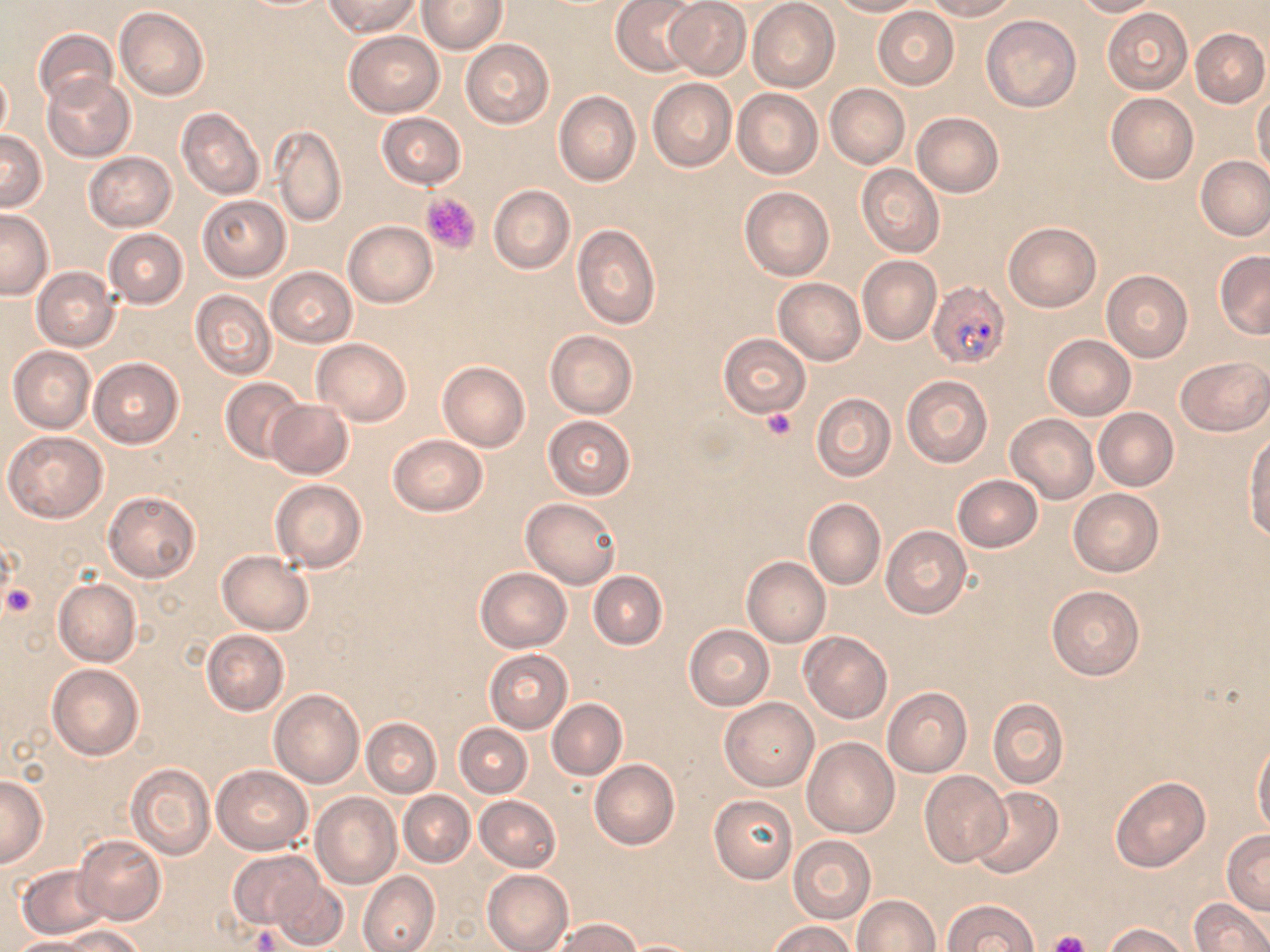

slide-level diagnosis = Plasmodium falciparum
modality = optical microscopy
magnification = 1000x
Plasmodium falciparum-infected red blood cell locations = approximate bounding boxes as [x1, y1, x2, y2] in pixels: [926, 280, 1012, 370]
stain = May-Grünwald-Giemsa
preparation = thin blood film
platelet locations = approximate bounding boxes as [x1, y1, x2, y2] in pixels: [420, 191, 482, 254], [761, 409, 797, 440], [3, 581, 35, 615], [1047, 930, 1090, 952]
image size = 1270×952 pixels
uninfected red blood cell locations = approximate bounding boxes as [x1, y1, x2, y2] in pixels: [322, 0, 419, 36], [418, 0, 507, 54], [612, 0, 700, 76], [828, 0, 924, 16], [924, 0, 1019, 20], [1071, 0, 1161, 17], [664, 1, 751, 80], [747, 1, 840, 92], [115, 6, 209, 100], [873, 6, 959, 90], [1102, 9, 1193, 94], [982, 15, 1080, 112], [1190, 27, 1269, 108], [35, 28, 117, 109], [344, 31, 444, 118], [460, 39, 555, 128], [0, 67, 11, 144], [42, 74, 136, 161], [647, 78, 737, 172], [825, 83, 910, 168], [732, 87, 824, 179], [554, 91, 641, 186], [1106, 92, 1199, 185], [1252, 92, 1270, 178], [177, 108, 264, 200], [375, 112, 467, 189], [912, 112, 1004, 198], [268, 125, 347, 227], [0, 129, 46, 210], [85, 151, 177, 231], [1196, 155, 1269, 241], [856, 164, 944, 258], [488, 185, 575, 274], [739, 186, 834, 280], [196, 193, 291, 281], [0, 209, 54, 299], [344, 220, 438, 307], [1004, 222, 1101, 312], [572, 224, 660, 328], [104, 229, 188, 308], [1215, 249, 1270, 339], [857, 256, 941, 345], [32, 266, 120, 351], [266, 266, 357, 347], [1101, 269, 1193, 362], [773, 276, 866, 366], [191, 291, 277, 380], [545, 330, 638, 418], [719, 333, 811, 418], [1043, 334, 1136, 420], [313, 338, 411, 425], [8, 345, 96, 433], [1176, 356, 1270, 437], [89, 357, 183, 448], [438, 361, 530, 452], [901, 374, 994, 468], [221, 376, 307, 464], [810, 392, 895, 482], [266, 400, 354, 479], [1094, 407, 1179, 491], [1006, 413, 1098, 504], [544, 415, 634, 499], [5, 430, 109, 523], [1244, 430, 1270, 538], [388, 434, 488, 516], [953, 475, 1042, 552], [270, 479, 366, 573], [1069, 488, 1164, 577], [103, 491, 201, 583], [522, 497, 622, 588], [803, 497, 885, 590], [881, 526, 971, 620], [218, 550, 313, 635], [741, 556, 830, 648], [475, 566, 571, 653], [588, 569, 667, 650], [53, 579, 141, 667], [1047, 586, 1144, 680], [685, 625, 773, 709], [202, 629, 289, 715], [799, 630, 892, 724], [485, 650, 572, 732], [46, 664, 144, 760], [883, 687, 972, 777], [270, 689, 364, 788], [987, 697, 1069, 789], [720, 698, 819, 790], [548, 699, 626, 780], [361, 717, 441, 797], [455, 723, 532, 797], [802, 737, 899, 837], [1253, 740, 1270, 837], [590, 760, 679, 850], [127, 765, 215, 860], [211, 765, 312, 854], [919, 771, 1011, 866], [0, 775, 49, 868], [1110, 776, 1210, 872], [970, 785, 1062, 878], [399, 790, 475, 868], [311, 791, 401, 889], [709, 793, 798, 883], [476, 795, 561, 872], [1222, 830, 1270, 913], [74, 834, 166, 925], [788, 835, 877, 923], [229, 851, 326, 930], [18, 865, 109, 939], [482, 869, 573, 952], [358, 871, 441, 952], [268, 877, 350, 950], [853, 896, 940, 952], [941, 898, 1039, 951], [1190, 898, 1269, 951], [553, 918, 642, 952], [768, 920, 856, 952], [1104, 923, 1190, 952], [48, 924, 145, 951], [4, 936, 102, 952]
field of view = one of a larger specimen